Comment on the morphology of the red blood cells.
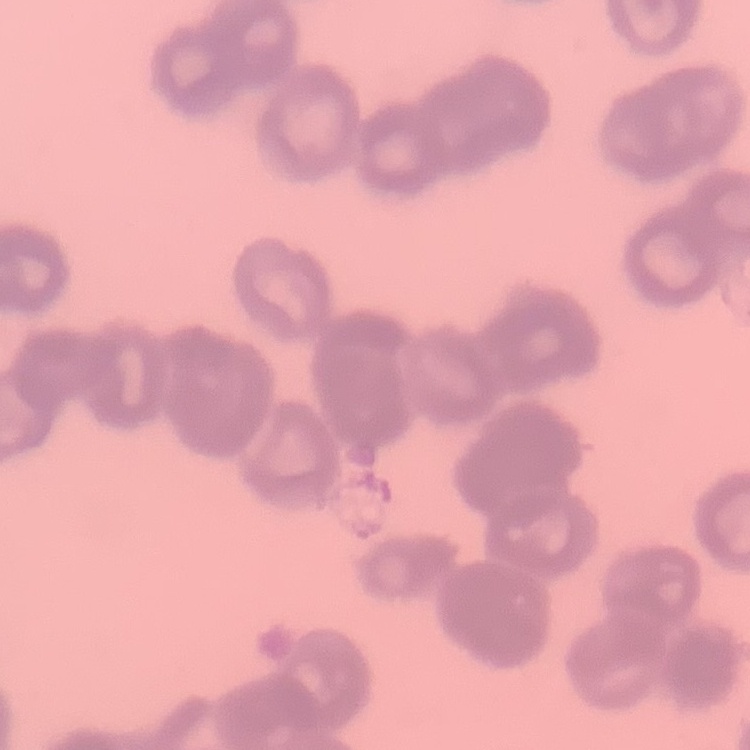

They show rouleaux formation.

stain = Field's or Giemsa
preparation = thin blood smear
image type = square crop of a larger photomicrograph